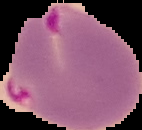
preparation = thin blood smear
image type = segmented cell region with the area outside set to black
malaria status = parasitized
image size = 142×130 pixels